Find the cells and give the type of each one.
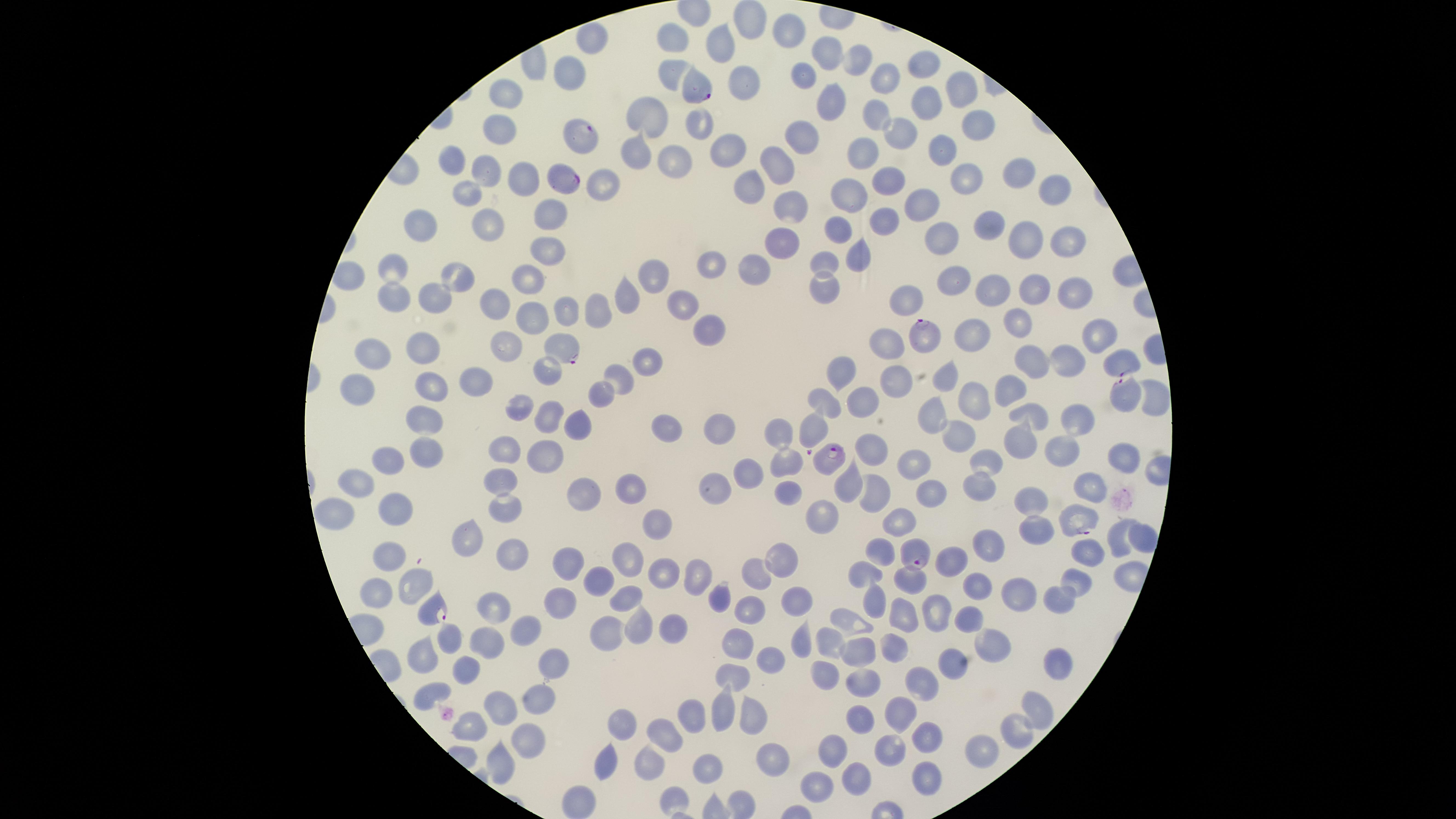
Approximate marker points as [x, y] in pixels.
Parasitized RBCs: [702, 89], [585, 134], [563, 181], [924, 338], [564, 351], [1124, 360], [1125, 396], [811, 432], [828, 462], [1079, 518], [915, 551], [433, 610].
Uninfected RBCs: [746, 19], [783, 36], [679, 38], [725, 40], [594, 41], [822, 50], [855, 60], [924, 60], [801, 73], [671, 75], [563, 76], [885, 76], [737, 86], [963, 86], [510, 98], [915, 103], [830, 105], [875, 108], [644, 113], [972, 122], [699, 127], [502, 128], [896, 129], [803, 138], [947, 148], [733, 150], [639, 153], [865, 154], [681, 159], [781, 161], [455, 162], [487, 167], [966, 171], [1017, 172], [527, 174], [604, 178], [885, 180], [756, 186], [1049, 190], [466, 194], [851, 194], [916, 201], [791, 209], [548, 217], [887, 218], [992, 227], [424, 228], [486, 229], [837, 231], [950, 240], [1023, 241], [781, 244], [1064, 244], [858, 249], [544, 255], [827, 256], [712, 265], [755, 266], [397, 270], [655, 271], [950, 276], [526, 279], [461, 280], [822, 285], [1035, 288], [992, 290], [1082, 290], [624, 295], [438, 300], [395, 302], [497, 302], [906, 302], [682, 308], [594, 309], [531, 312], [559, 312], [1017, 319], [706, 330], [1097, 334], [972, 335], [887, 343], [421, 344], [511, 347], [371, 356], [1031, 358], [1066, 360], [649, 362], [847, 366], [470, 373], [543, 374], [619, 374], [904, 375], [945, 375], [358, 383], [422, 386], [1008, 387], [601, 397], [860, 397], [827, 402], [521, 404], [970, 405], [936, 410], [1037, 411], [545, 415], [428, 421], [579, 423], [1072, 426], [664, 429], [776, 429], [955, 430], [720, 431], [1013, 443], [426, 449], [869, 450], [1060, 450], [508, 451], [1126, 455], [546, 457], [986, 459], [788, 463], [387, 464], [918, 466], [751, 471], [502, 472], [979, 483], [1089, 483], [850, 486], [628, 488], [928, 489], [364, 490], [719, 490], [783, 493], [580, 494], [873, 498], [1029, 504], [506, 508], [396, 509], [336, 513], [827, 517], [658, 520], [897, 522], [1039, 529], [1114, 533], [1142, 533], [465, 536], [988, 547], [1095, 549], [507, 551], [876, 555], [628, 558], [956, 558], [391, 561], [785, 563], [570, 564], [696, 573], [752, 573], [862, 574], [1082, 577], [915, 580], [594, 581], [418, 583], [976, 585], [1023, 593], [376, 594], [797, 594], [873, 594], [1062, 596], [625, 597], [717, 597], [493, 603], [555, 604], [750, 609], [901, 612], [931, 613], [966, 619], [848, 624], [636, 626], [527, 627], [600, 633], [453, 636], [798, 637], [738, 640], [487, 642], [831, 643], [990, 645], [897, 646], [858, 651], [419, 655], [768, 655], [952, 655], [556, 664], [1056, 664], [461, 668], [826, 673], [735, 674], [861, 680], [922, 680], [423, 694], [541, 696], [721, 701], [501, 706], [900, 706], [1032, 709], [690, 715], [623, 721], [756, 721], [855, 725], [664, 733], [1008, 733], [471, 734], [927, 735], [526, 739], [888, 748], [978, 749], [833, 753], [773, 755], [647, 762], [710, 765], [494, 770], [604, 770], [861, 775], [928, 778], [820, 784], [676, 793], [582, 797].
No WBCs identified.

Summary:
  - Preparation: thin blood smear
  - Capture: smartphone photograph through the microscope eyepiece
  - Visible region: circular
  - Field of view: single
  - Species: Plasmodium falciparum
  - Stain: Giemsa
  - Image size: 1456×819 pixels